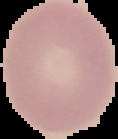

Result: negative for Plasmodium parasites. Image is 118×139 pixels. Segmented cell region on a black background. From a thin blood film.